Assess this cell for malaria.
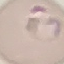

It is parasitized.

{
  "preparation": "thin smear",
  "image_type": "cell patch, automatically extracted from a larger field of view and resized to 64 × 64 pixels",
  "capture": "smartphone camera at the microscope eyepiece",
  "stain": "Giemsa"
}